Assess the morphology of the erythrocytes.
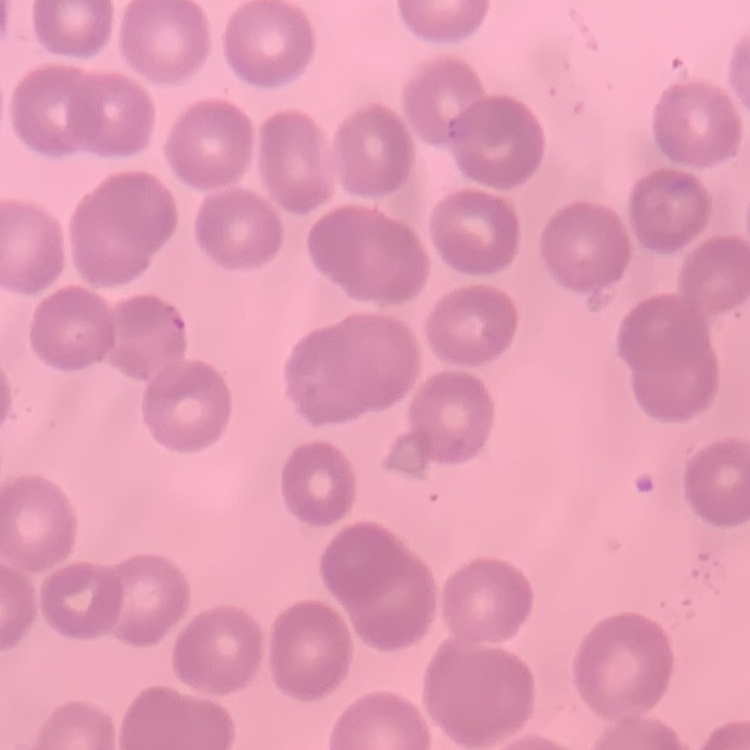
No rouleaux formation.

Summary:
  - Image type: one tile cut from a larger photomicrograph
  - Preparation: thin blood smear
  - Stain: Field's or Giemsa